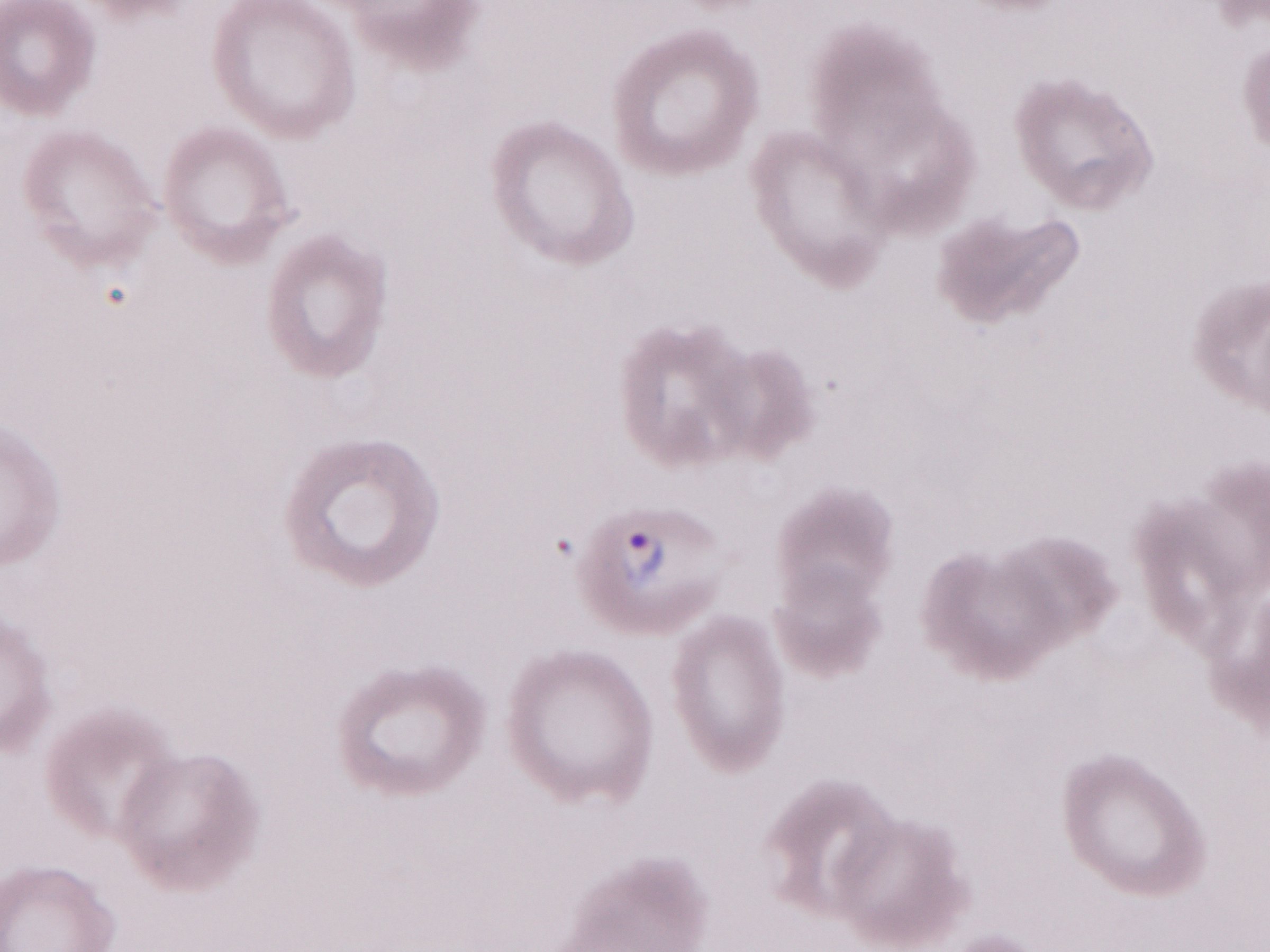 Thin peripheral-blood smear. Single field of view. May-Grünwald-Giemsa stain. Olympus BX43 microscope, Olympus DP73 camera. 1,000x magnification. Image is 1270×952 pixels. Patient-level malaria diagnosis: positive.